Report the malaria status of this cell.
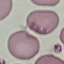

Uninfected.

capture: smartphone through the microscope eyepiece
preparation: thin blood smear
image_type: automatically extracted cell patch, resized to 64 × 64 pixels
stain: Giemsa